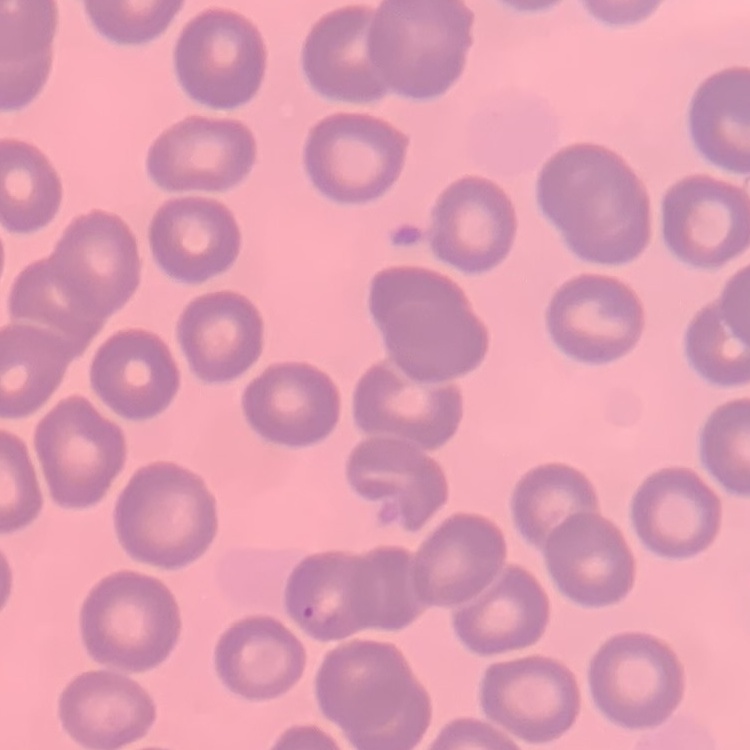

Summary:
  - Red blood cell morphology: no rouleaux formation
  - Preparation: thin blood film
  - Image type: square crop of a larger photomicrograph
  - Stain: Field's or Giemsa